State which cell type is depicted.
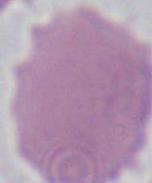
This is an erythrocyte.

Summary:
  - Magnification: 1000x
  - Modality: micrograph